Report the malaria status of this cell.
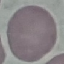

Uninfected.

stain = Giemsa
preparation = thin blood smear
image type = automatically extracted cell patch, resized to 64 × 64 pixels
capture = smartphone camera at the microscope eyepiece